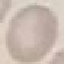
Result: no malaria parasites seen. Giemsa stain. Cell patch, automatically extracted from a larger field of view and resized to 64 × 64 pixels. Acquired by smartphone through the microscope eyepiece. Thin blood smear.